Assess this cell for malaria.
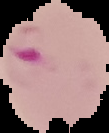

It is parasitized.

Segmented cell region on a black background. Image is 109×133 pixels. From a thin blood film.